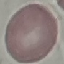

malaria_status: uninfected
capture: smartphone camera at the microscope eyepiece
image_type: automatically extracted cell patch, resized to 64 × 64 pixels
preparation: thin blood film
stain: Giemsa